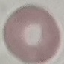
result: no malaria parasites detected
stain: Giemsa
image_type: cell patch, automatically extracted from a larger field of view and resized to 64 × 64 pixels
preparation: thin blood smear
capture: smartphone through the microscope eyepiece